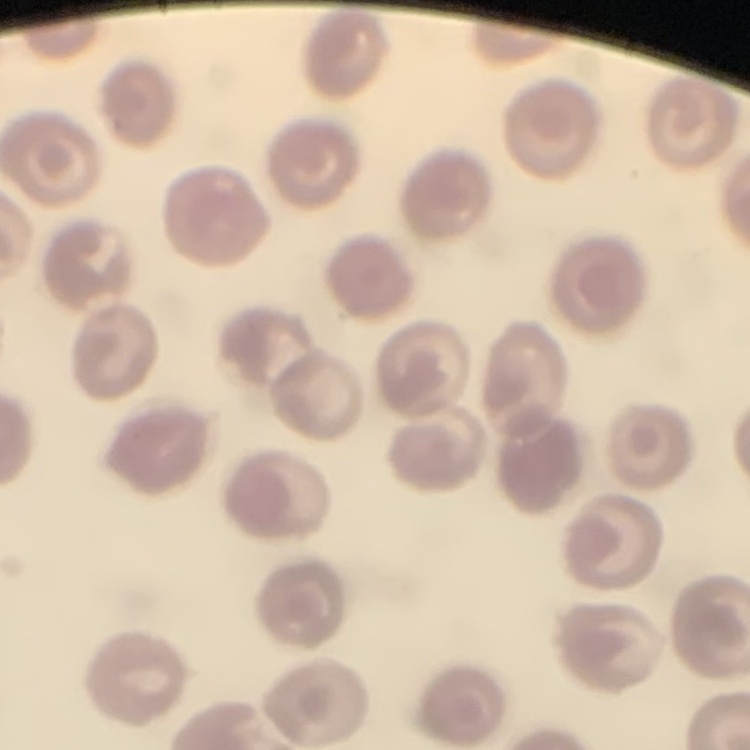
Summary:
  - Erythrocyte morphology: no rouleaux formation
  - Stain: Field's or Giemsa
  - Preparation: thin blood film
  - Image type: one tile cut from a larger photomicrograph